Assess this cell for malaria.
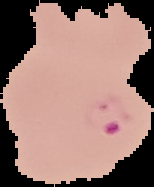

It is parasitized.

image size = 154×187 pixels
preparation = thin blood film
image type = segmented cell region with the area outside set to black